Identify the blood parasite species.
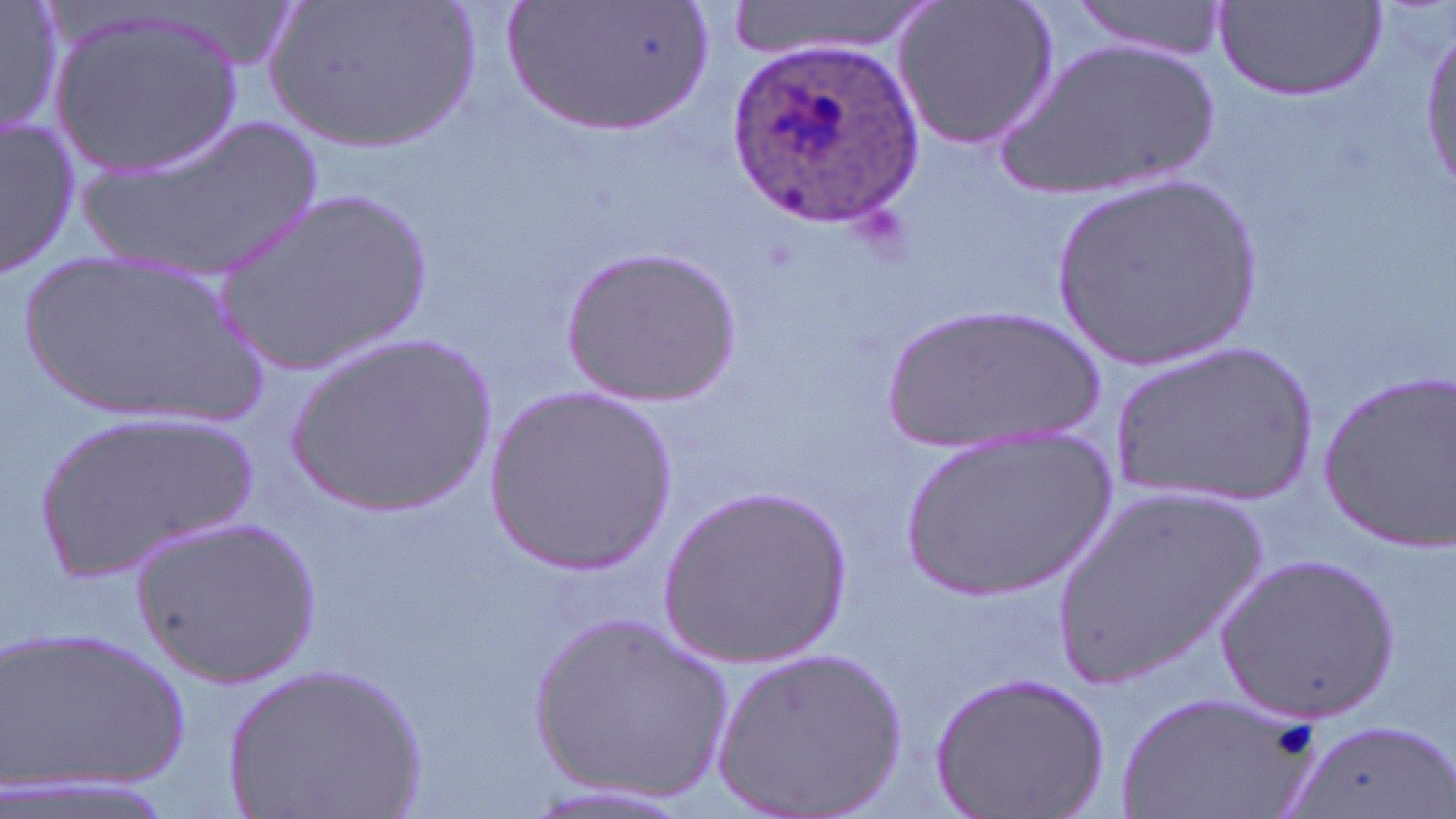

Plasmodium ovale.

preparation = thin blood film
field of view = single
stain = May-Grünwald-Giemsa
uninfected red blood cell locations = approximate bounding boxes as named x1/y1/x2/y2 corners in pixels: (x1=1, y1=0, x2=64, y2=140), (x1=267, y1=0, x2=484, y2=154), (x1=718, y1=0, x2=939, y2=65), (x1=892, y1=0, x2=1059, y2=152), (x1=1067, y1=0, x2=1231, y2=61), (x1=507, y1=1, x2=708, y2=134), (x1=1216, y1=3, x2=1385, y2=102), (x1=50, y1=6, x2=245, y2=180), (x1=1415, y1=27, x2=1454, y2=196), (x1=994, y1=34, x2=1223, y2=201), (x1=81, y1=112, x2=330, y2=280), (x1=2, y1=116, x2=80, y2=277), (x1=1047, y1=174, x2=1265, y2=373), (x1=209, y1=184, x2=440, y2=376), (x1=560, y1=246, x2=740, y2=407), (x1=11, y1=254, x2=266, y2=422), (x1=880, y1=303, x2=1112, y2=459), (x1=283, y1=334, x2=499, y2=517), (x1=1111, y1=340, x2=1324, y2=511), (x1=1315, y1=368, x2=1456, y2=555), (x1=481, y1=383, x2=678, y2=574), (x1=28, y1=408, x2=264, y2=584), (x1=896, y1=425, x2=1119, y2=601), (x1=1043, y1=481, x2=1274, y2=691), (x1=660, y1=483, x2=853, y2=669), (x1=132, y1=514, x2=321, y2=688), (x1=1214, y1=552, x2=1400, y2=721), (x1=525, y1=612, x2=739, y2=803), (x1=1, y1=622, x2=191, y2=804), (x1=715, y1=644, x2=912, y2=817), (x1=221, y1=662, x2=426, y2=819), (x1=932, y1=669, x2=1111, y2=819), (x1=1118, y1=690, x2=1320, y2=819), (x1=1290, y1=721, x2=1447, y2=819)
image size = 1456×819 pixels
modality = optical microscopy
Plasmodium ovale-infected red blood cell locations = approximate bounding boxes as named x1/y1/x2/y2 corners in pixels: (x1=725, y1=33, x2=919, y2=233)
magnification = 1000x